State the blood parasite species.
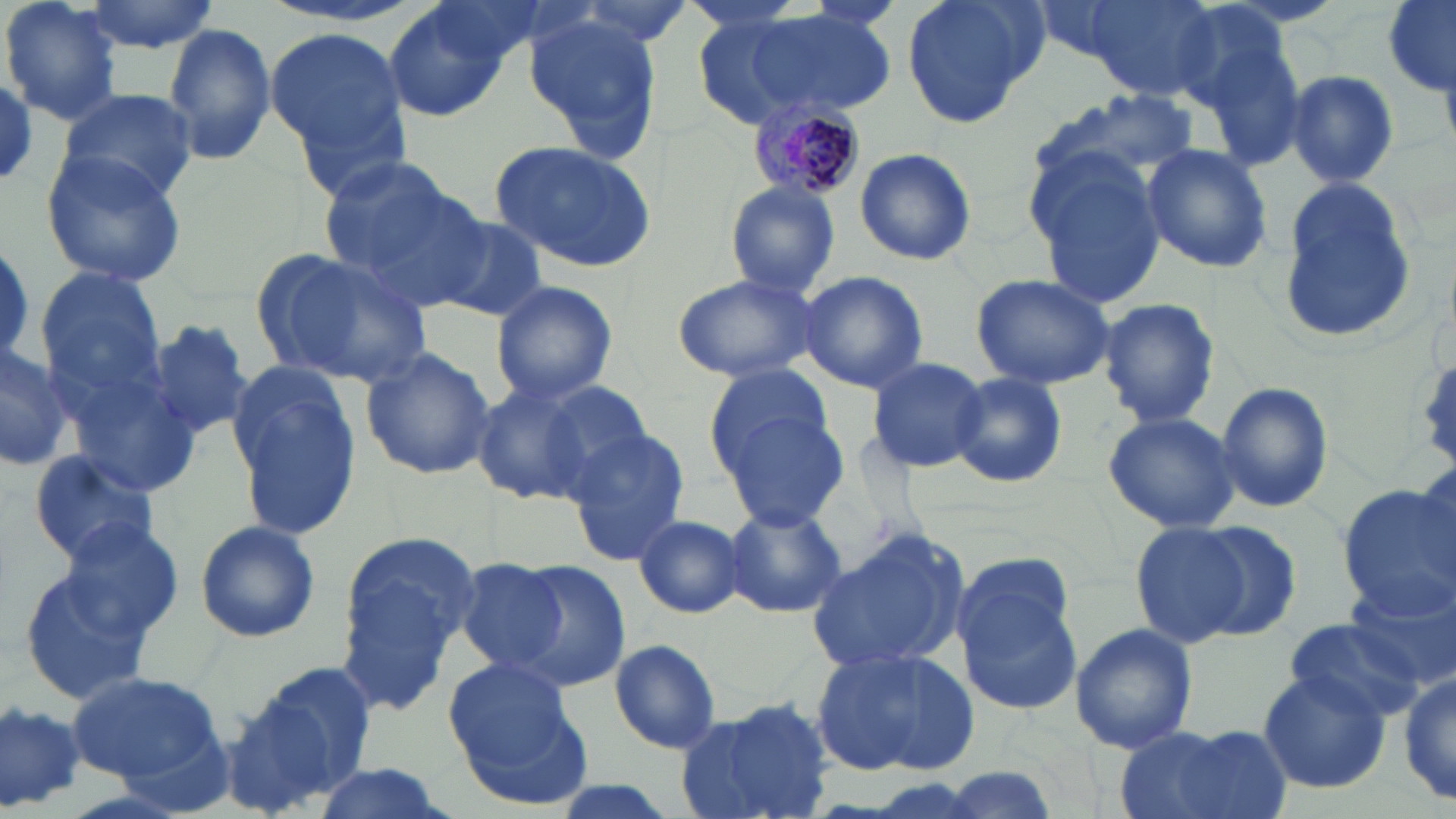
Plasmodium malariae.

preparation = thin blood film
uninfected red blood cell locations = approximate bounding boxes as (x1, y1, x2, y2) in pixels: (2, 0, 122, 127), (80, 0, 221, 52), (902, 0, 1046, 129), (1083, 0, 1225, 100), (1382, 2, 1456, 99), (386, 3, 512, 124), (741, 7, 898, 121), (519, 11, 667, 161), (161, 22, 278, 167), (264, 28, 410, 174), (1283, 69, 1401, 188), (0, 73, 37, 184), (60, 88, 197, 203), (1032, 89, 1205, 196), (488, 141, 658, 272), (1139, 143, 1274, 273), (852, 147, 977, 266), (1023, 147, 1173, 306), (40, 150, 188, 286), (315, 154, 472, 290), (1274, 176, 1423, 346), (725, 180, 841, 298), (429, 216, 550, 323), (0, 239, 34, 371), (255, 248, 434, 391), (35, 267, 166, 406), (798, 270, 929, 393), (669, 272, 819, 381), (970, 272, 1118, 389), (490, 279, 619, 404), (1097, 297, 1221, 427), (141, 320, 258, 440), (0, 337, 78, 474), (360, 346, 495, 481), (865, 356, 990, 473), (225, 363, 365, 539), (704, 364, 838, 475), (71, 372, 207, 496), (948, 373, 1068, 490), (472, 378, 596, 504), (535, 378, 659, 495), (1215, 382, 1335, 513), (713, 403, 849, 533), (1101, 410, 1243, 534), (561, 427, 691, 563), (28, 449, 162, 567), (1336, 482, 1455, 615), (722, 505, 846, 619), (632, 514, 747, 620), (52, 518, 187, 650), (193, 519, 321, 643), (1184, 520, 1305, 641), (1129, 521, 1254, 649), (804, 528, 972, 678), (339, 535, 484, 664), (17, 551, 171, 707), (500, 559, 632, 690), (954, 559, 1088, 718), (457, 561, 572, 675), (1346, 577, 1455, 691), (1281, 615, 1426, 722), (1069, 623, 1199, 756), (607, 638, 723, 754), (811, 647, 980, 778), (440, 655, 589, 800), (225, 656, 377, 809), (65, 669, 226, 785), (1400, 669, 1456, 806), (1256, 670, 1392, 795), (0, 698, 87, 815), (676, 701, 835, 819), (1118, 724, 1290, 819), (306, 764, 456, 819)
stain = May-Grünwald-Giemsa
field of view = single
modality = optical microscopy
image size = 1456×819 pixels
Plasmodium malariae-infected red blood cell locations = approximate bounding boxes as (x1, y1, x2, y2) in pixels: (748, 103, 866, 201)
magnification = 1000x